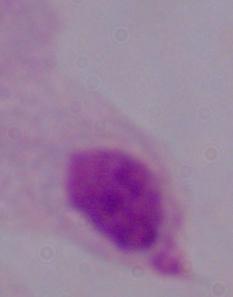
Summary:
  - Magnification: 1000x
  - Identification: trichomonad
  - Modality: photomicrograph